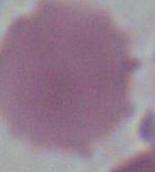
identification: erythrocyte
magnification: 1000x
modality: micrograph